Report the malaria status of this cell.
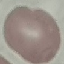

It is uninfected.

Summary:
  - Stain: Giemsa
  - Preparation: thin blood film
  - Image type: cell patch, automatically extracted from a larger field of view and resized to 64 × 64 pixels
  - Capture: smartphone camera at the microscope eyepiece